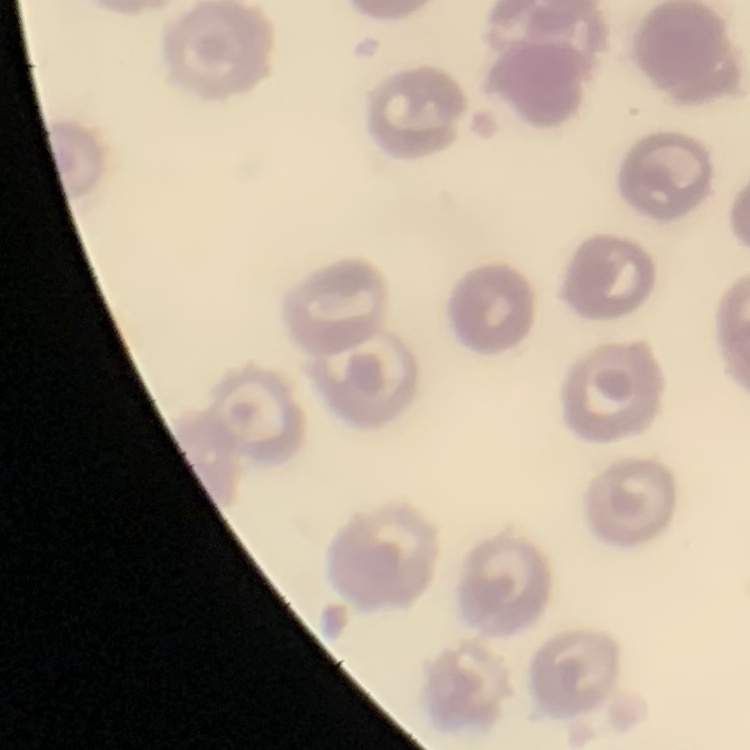
The red blood cells exhibit no rouleaux formation. Square crop of a larger photomicrograph. Field's or Giemsa stain. Thin blood film.